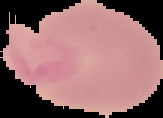

Summary:
  - Image size: 163×118 pixels
  - Image type: segmented cell region with the area outside set to black
  - Result: no malaria parasites seen
  - Preparation: thin blood smear